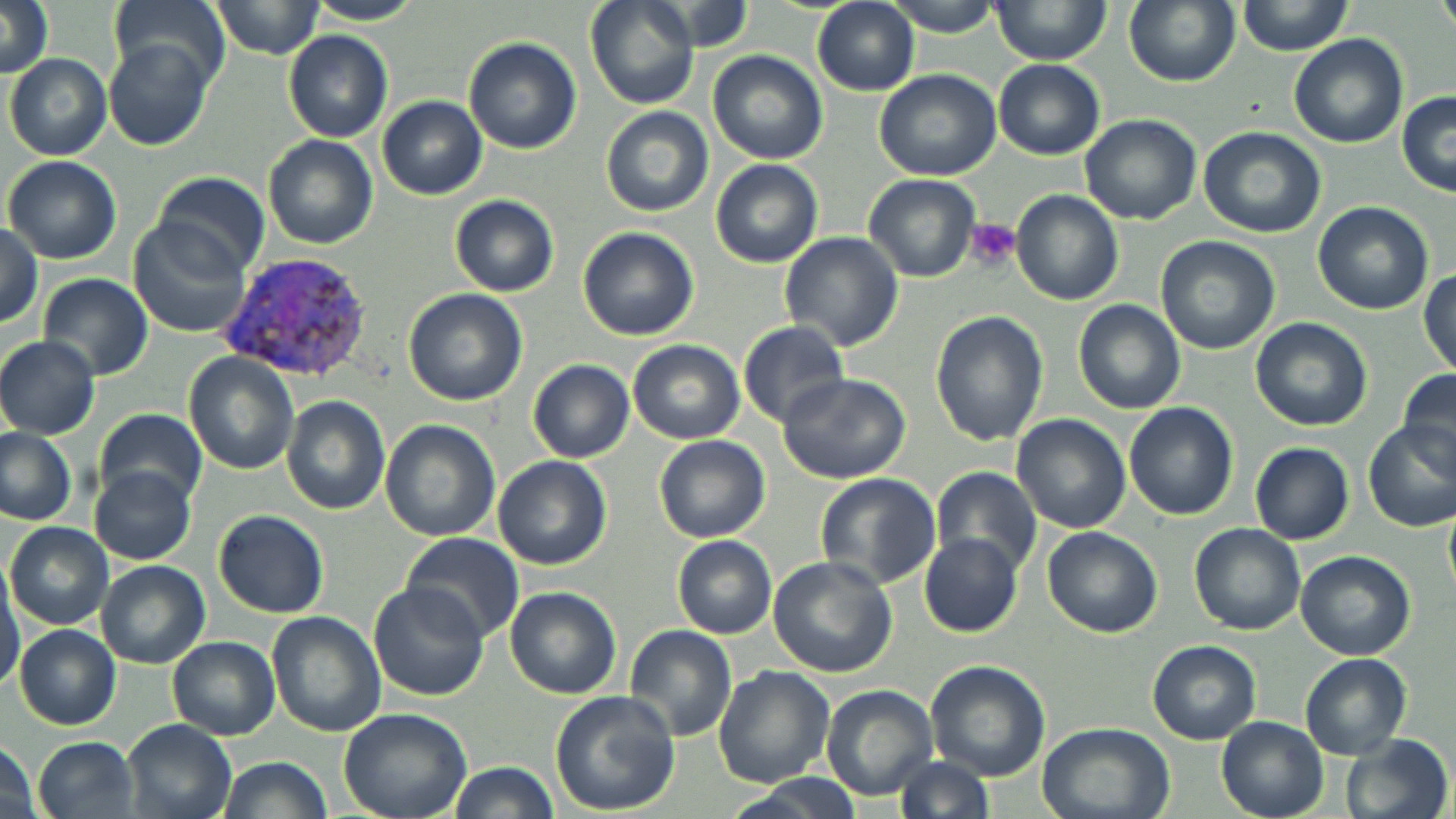

slide-level diagnosis = Plasmodium vivax
platelet locations = approximate bounding boxes as [x1, y1, x2, y2] in pixels: [964, 219, 1020, 270]
modality = optical microscopy
stain = May-Grünwald-Giemsa
image size = 1456×819 pixels
Plasmodium vivax-infected red blood cell locations = approximate bounding boxes as [x1, y1, x2, y2] in pixels: [217, 250, 372, 380]
magnification = 1000x
preparation = thin blood film
uninfected red blood cell locations = approximate bounding boxes as [x1, y1, x2, y2] in pixels: [0, 0, 54, 79], [110, 0, 230, 84], [205, 0, 325, 58], [304, 0, 428, 26], [587, 0, 698, 110], [812, 0, 918, 94], [885, 0, 1001, 37], [990, 0, 1112, 64], [1123, 0, 1241, 87], [1236, 0, 1352, 56], [647, 1, 759, 50], [284, 30, 392, 143], [1288, 35, 1409, 150], [463, 37, 582, 153], [105, 41, 214, 150], [708, 50, 828, 165], [6, 54, 112, 160], [994, 60, 1105, 159], [875, 69, 1001, 180], [1396, 92, 1456, 196], [377, 95, 485, 199], [601, 106, 713, 217], [1081, 114, 1201, 224], [1198, 126, 1325, 239], [264, 135, 377, 247], [2, 155, 121, 264], [711, 160, 823, 268], [156, 172, 270, 278], [862, 173, 980, 282], [1010, 190, 1123, 307], [450, 195, 558, 296], [1313, 201, 1434, 314], [0, 220, 43, 331], [128, 220, 253, 337], [578, 226, 699, 340], [778, 231, 904, 353], [1156, 235, 1280, 355], [1417, 268, 1455, 376], [38, 272, 153, 381], [403, 288, 528, 406], [1074, 300, 1187, 414], [930, 311, 1047, 446], [1249, 316, 1375, 432], [736, 319, 849, 426], [0, 335, 101, 438], [627, 339, 746, 443], [185, 351, 300, 474], [529, 360, 635, 462], [1397, 369, 1455, 464], [775, 372, 913, 484], [282, 397, 389, 514], [1124, 401, 1238, 520], [95, 407, 210, 505], [1012, 414, 1130, 534], [379, 420, 501, 543], [1363, 421, 1456, 530], [0, 427, 78, 524], [655, 434, 770, 543], [1250, 441, 1355, 544], [494, 455, 611, 570], [930, 465, 1045, 574], [89, 469, 195, 563], [812, 472, 943, 591], [1444, 505, 1456, 597], [212, 508, 329, 618], [6, 522, 113, 629], [1190, 523, 1306, 635], [1043, 527, 1162, 638], [400, 531, 524, 641], [672, 536, 776, 638], [919, 536, 1022, 637], [1295, 550, 1416, 659], [766, 555, 898, 678], [96, 561, 210, 668], [0, 569, 22, 692], [369, 582, 487, 700], [505, 586, 622, 698], [268, 612, 385, 736], [15, 624, 120, 729], [624, 625, 736, 742], [169, 636, 279, 740], [1148, 640, 1261, 743], [1300, 653, 1413, 759], [925, 661, 1052, 782], [716, 666, 836, 787], [822, 685, 937, 801], [548, 691, 681, 815], [339, 708, 471, 819], [1215, 716, 1328, 818], [124, 720, 237, 819], [1036, 722, 1173, 819], [1339, 734, 1452, 819], [31, 735, 140, 818], [0, 736, 44, 819], [897, 754, 993, 819], [217, 756, 334, 819], [447, 760, 558, 819], [714, 775, 861, 819]
field of view = single